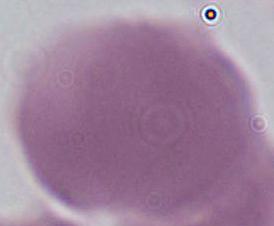
Summary:
  - Identification: red blood cell
  - Modality: photomicrograph
  - Magnification: 1000x